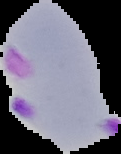
malaria_status: parasitized
image_type: segmented cell region with the area outside set to black
image_size: 121×154 pixels
preparation: thin blood smear